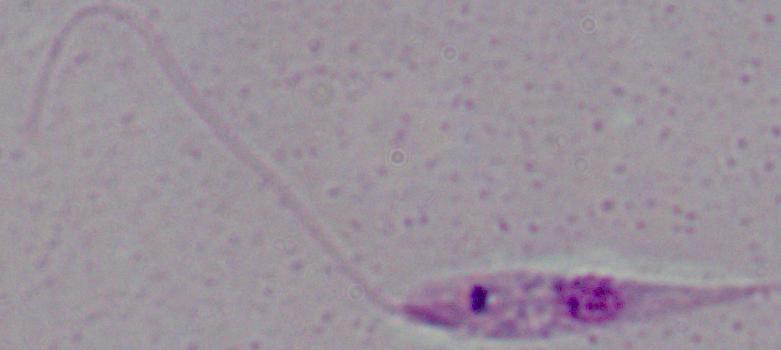 Photomicrograph. A Leishmania parasite is shown. Captured at 1000x magnification.